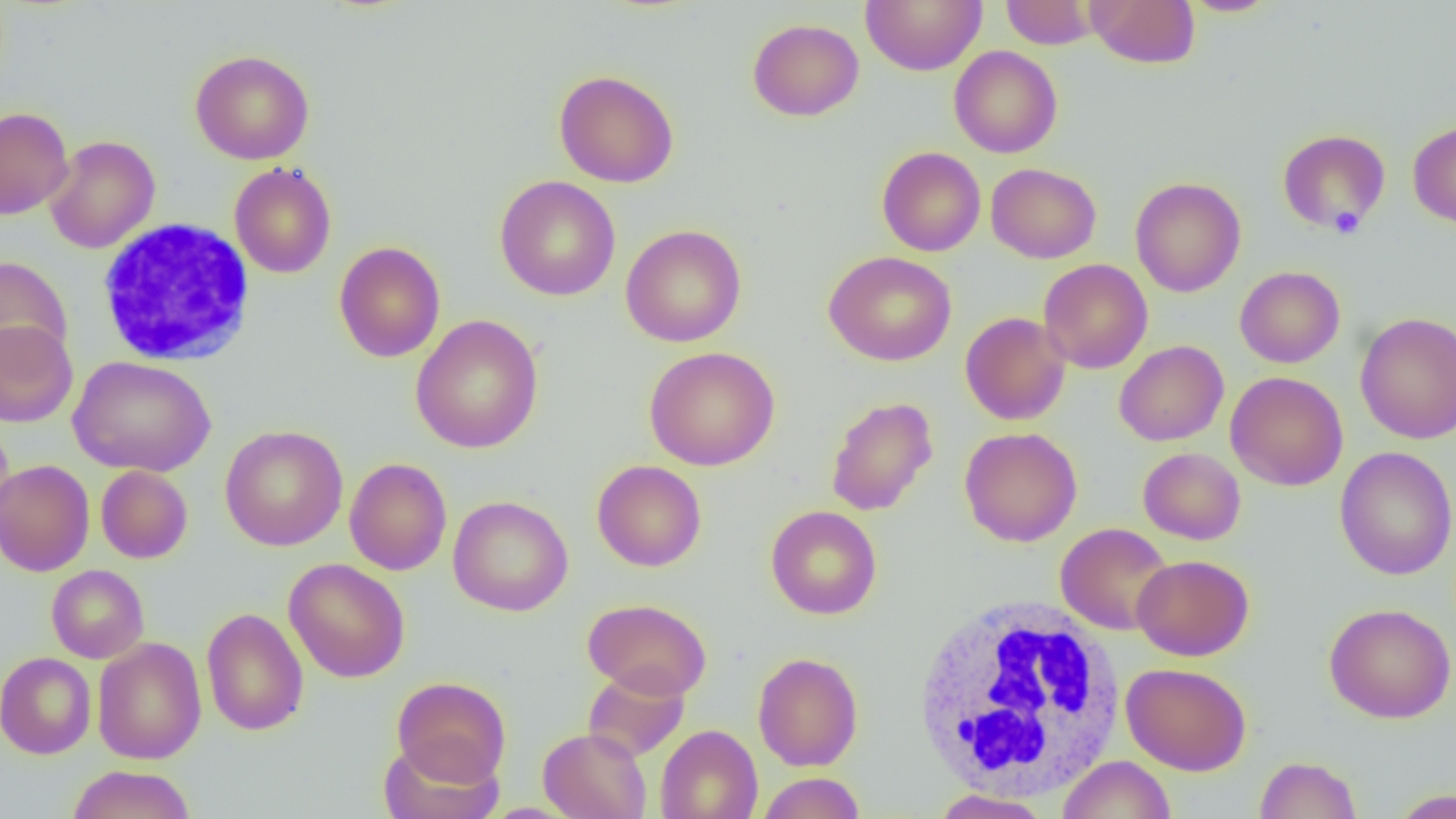
slide-level diagnosis = negative for blood parasites
platelet locations = approximate bounding boxes as [x1, y1, x2, y2] in pixels: [1329, 205, 1365, 238]
modality = light microscopy
preparation = thin blood smear
magnification = 1000x
image size = 1456×819 pixels
field of view = single
uninfected red blood cell locations = approximate bounding boxes as [x1, y1, x2, y2] in pixels: [860, 0, 986, 75], [1001, 0, 1099, 49], [1086, 0, 1200, 68], [1178, 0, 1282, 17], [747, 18, 864, 121], [949, 45, 1062, 158], [190, 49, 315, 165], [553, 70, 679, 187], [0, 107, 74, 220], [1408, 120, 1456, 229], [1277, 129, 1391, 234], [45, 135, 160, 253], [877, 147, 986, 256], [229, 161, 337, 279], [986, 163, 1101, 264], [494, 176, 621, 301], [1130, 177, 1246, 297], [620, 224, 747, 347], [333, 241, 446, 362], [823, 250, 957, 367], [0, 255, 72, 368], [1038, 259, 1153, 374], [1235, 266, 1345, 368], [960, 312, 1071, 425], [1355, 312, 1456, 444], [410, 314, 544, 454], [0, 319, 79, 427], [1114, 340, 1229, 446], [644, 346, 781, 471], [68, 356, 216, 477], [1225, 372, 1348, 491], [825, 396, 939, 516], [0, 423, 14, 533], [220, 425, 348, 551], [959, 427, 1082, 547], [1335, 446, 1456, 580], [1138, 447, 1246, 544], [344, 458, 452, 576], [0, 459, 95, 576], [592, 460, 707, 571], [96, 465, 193, 563], [447, 495, 573, 616], [765, 505, 882, 620], [1055, 522, 1174, 635], [1132, 554, 1254, 661], [284, 558, 410, 683], [46, 565, 149, 663], [582, 598, 712, 700], [1324, 603, 1456, 723], [201, 608, 309, 736], [92, 637, 207, 764], [0, 652, 97, 759], [753, 652, 864, 771], [1121, 662, 1251, 775], [582, 667, 690, 762], [391, 676, 512, 785], [655, 725, 763, 819], [537, 727, 652, 819], [378, 738, 503, 819], [1057, 754, 1176, 819], [1254, 755, 1362, 819], [66, 764, 196, 819], [757, 772, 866, 818], [931, 788, 1051, 819], [1389, 788, 1455, 818]
white blood cell locations = approximate bounding boxes as [x1, y1, x2, y2] in pixels: [96, 218, 256, 368], [913, 596, 1126, 800]